Assess this cell for malaria.
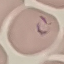

It is parasitized.

stain = Giemsa
capture = smartphone camera at the microscope eyepiece
image type = cell patch, automatically extracted from a larger field of view and resized to 64 × 64 pixels
preparation = thin blood smear